Classify this cell by malaria status.
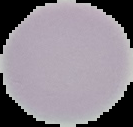

It is uninfected.

From a thin blood smear. Cell region segmented out of the field of view; the surrounding area is masked to black. Image is 133×127 pixels.